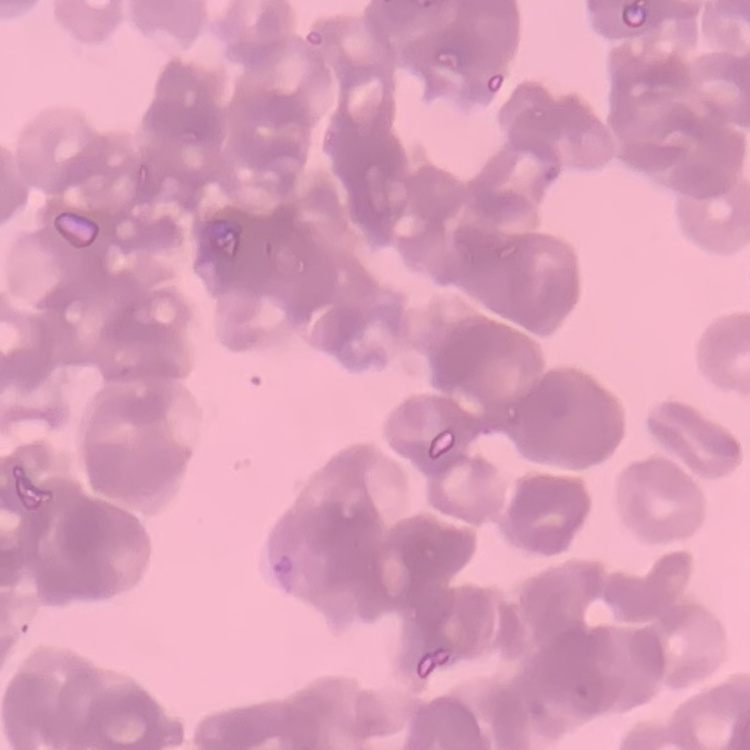 The erythrocytes show rouleaux formation. One tile cut from a larger photomicrograph. Thin blood smear. Field's or Giemsa stain.